Describe the morphology of the red blood cells.
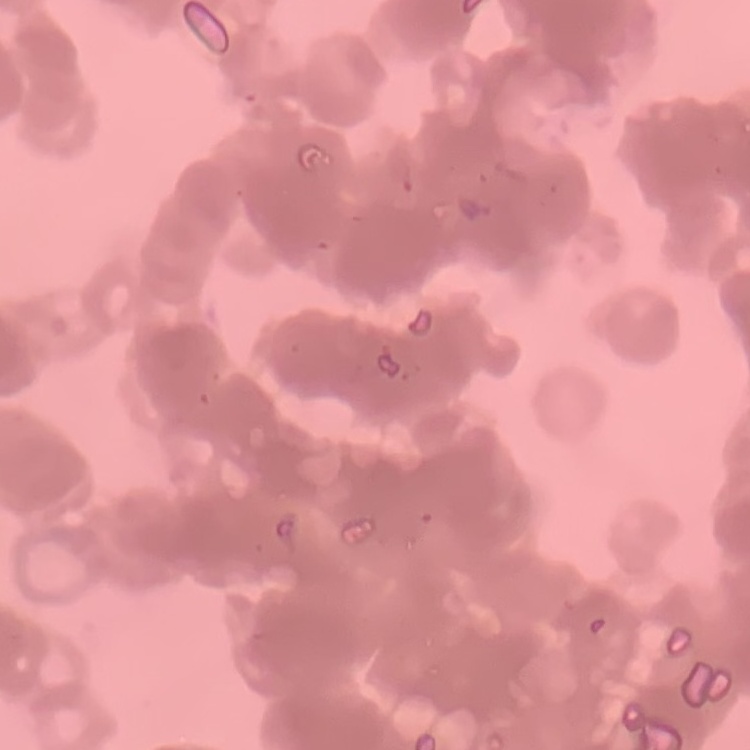

Rouleaux formation.

stain = Field's or Giemsa
image type = square crop of a larger photomicrograph
preparation = thin blood film